Give the extent of all Plasmodium falciparum-infected red blood cells.
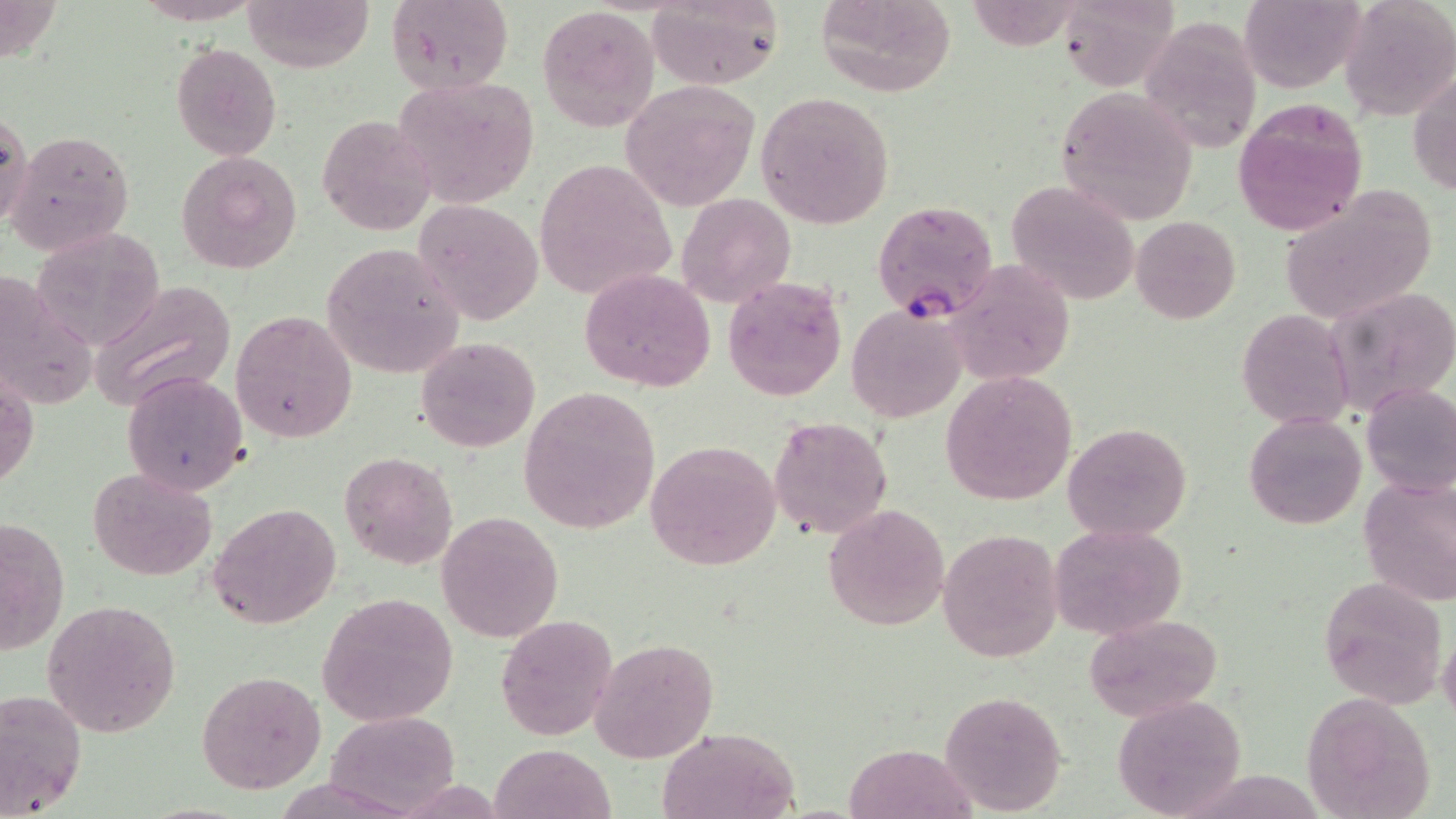

Approximate bounding boxes as (x1, y1, x2, y2) in pixels.
Plasmodium falciparum-infected red blood cells: (872, 201, 997, 321).

slide_level_diagnosis: Plasmodium falciparum
preparation: thin blood smear
uninfected_red_blood_cell_locations: 'approximate bounding boxes as (x1, y1, x2, y2) in pixels: (244, 0, 376, 71), (814, 0, 958, 96), (965, 0, 1090, 52), (1054, 0, 1179, 89), (1240, 0, 1364, 94), (384, 1, 514, 93), (646, 1, 784, 89), (1342, 1, 1455, 120), (536, 4, 660, 134), (1140, 17, 1266, 151), (171, 42, 282, 160), (1409, 67, 1456, 197), (391, 74, 541, 209), (619, 78, 763, 213), (1053, 87, 1199, 225), (755, 91, 895, 229), (1230, 97, 1368, 237), (1, 106, 32, 231), (317, 113, 437, 238), (7, 130, 136, 254), (175, 151, 302, 274), (535, 159, 675, 303), (1006, 178, 1140, 305), (1277, 187, 1438, 326), (692, 191, 815, 391), (677, 193, 795, 307), (416, 199, 545, 326), (1131, 216, 1241, 323), (29, 228, 166, 351), (320, 243, 463, 380), (944, 260, 1074, 386), (578, 269, 716, 391), (0, 275, 96, 415), (722, 275, 847, 401), (86, 282, 238, 411), (1326, 284, 1456, 416), (847, 304, 965, 424), (1237, 308, 1357, 431), (232, 311, 358, 442), (415, 336, 540, 453), (1, 367, 38, 494), (121, 369, 249, 496), (939, 370, 1078, 506), (1361, 383, 1456, 499), (518, 386, 661, 533), (1244, 413, 1366, 530), (769, 415, 892, 540), (1063, 422, 1192, 541), (645, 440, 782, 572), (339, 451, 458, 571), (87, 468, 218, 582), (1357, 472, 1456, 606), (209, 501, 342, 630), (824, 502, 949, 632), (436, 511, 564, 642), (1, 516, 70, 654), (1048, 522, 1186, 639), (938, 528, 1063, 662), (1318, 576, 1447, 708), (318, 593, 459, 726), (44, 599, 181, 736), (495, 614, 618, 741), (1085, 614, 1224, 722), (589, 638, 718, 762), (197, 671, 327, 792), (0, 687, 86, 819), (939, 688, 1068, 816), (1302, 692, 1437, 818), (1111, 693, 1248, 818), (326, 710, 460, 817), (656, 727, 802, 819), (845, 741, 976, 819), (490, 743, 615, 819)'
image_size: 1456×819 pixels
modality: light microscopy
field_of_view: single
stain: May-Grünwald-Giemsa
magnification: 1000x